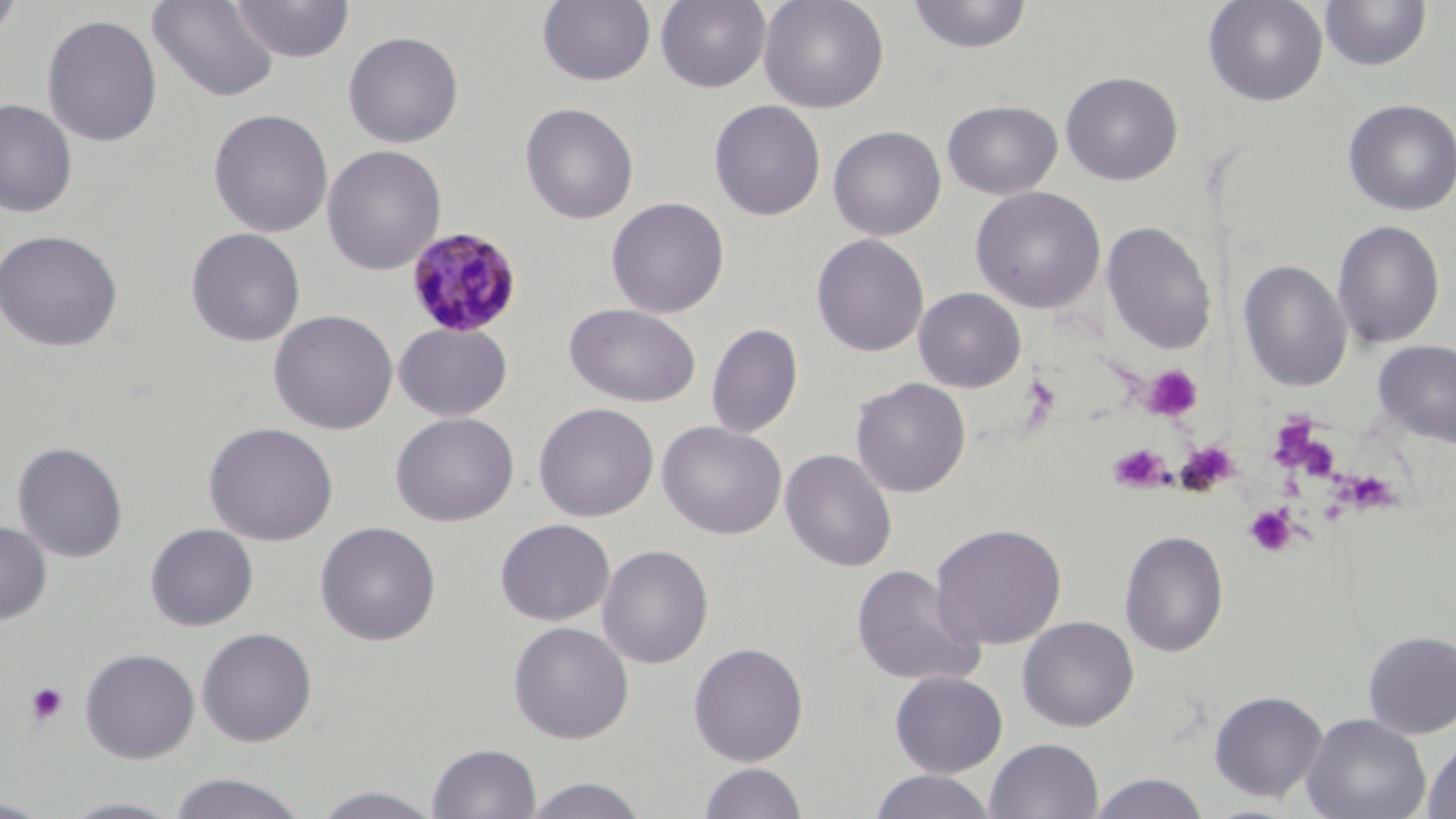

Summary:
  - Coordinate format: approximate bounding boxes as (x1,y1)-(x2,y2) corner pairs in pixels
  - Platelet locations: (1141,363)-(1203,422), (1020,374)-(1061,423), (1264,415)-(1341,482), (1175,439)-(1240,496), (1108,443)-(1169,493), (1346,474)-(1402,517), (1244,504)-(1298,557), (25,681)-(69,726)
  - Plasmodium malariae-infected red blood cell locations: (405,225)-(523,338)
  - Uninfected red blood cell locations: (0,0)-(23,47), (230,0)-(355,63), (536,0)-(656,86), (656,0)-(771,92), (758,0)-(889,114), (906,0)-(1033,54), (1203,0)-(1329,107), (147,1)-(280,103), (1319,1)-(1431,71), (41,13)-(163,149), (342,30)-(464,148), (1060,71)-(1183,185), (940,92)-(1184,191), (1342,98)-(1456,216), (0,99)-(78,218), (709,99)-(826,221), (942,99)-(1063,200), (519,102)-(639,224), (208,108)-(333,237), (827,125)-(946,240), (321,144)-(447,275), (970,186)-(1106,313), (605,197)-(730,318), (1332,219)-(1446,348), (1101,220)-(1217,354), (185,227)-(306,347), (0,229)-(123,352), (811,233)-(929,357), (1238,259)-(1352,392), (913,287)-(1026,392), (564,303)-(702,407), (268,309)-(398,435), (393,322)-(512,421), (705,322)-(804,438), (1372,339)-(1456,447), (850,377)-(971,498), (533,402)-(659,522), (390,412)-(519,526), (657,420)-(787,540), (203,421)-(339,546), (12,441)-(128,563), (780,448)-(897,572), (495,518)-(615,626), (0,520)-(52,624), (315,521)-(441,646), (930,522)-(1067,650), (145,523)-(258,631), (1118,530)-(1229,657), (597,544)-(714,669), (851,563)-(986,687), (1017,615)-(1139,731), (508,621)-(634,744), (196,626)-(318,747), (1362,629)-(1456,739), (688,642)-(809,766), (79,647)-(200,764), (889,670)-(1009,778), (1208,690)-(1328,802), (1301,713)-(1431,819), (1422,735)-(1456,819), (985,737)-(1103,819), (426,741)-(542,819), (698,761)-(808,819), (868,770)-(998,819), (167,772)-(311,819), (1088,772)-(1211,818), (521,776)-(649,819), (309,784)-(445,818), (58,795)-(187,818), (0,797)-(58,818)
  - Slide-level diagnosis: Plasmodium malariae
  - Modality: light microscopy
  - Image size: 1456×819 pixels
  - Stain: May-Grünwald-Giemsa
  - Preparation: thin blood film
  - Magnification: 1000x
  - Field of view: single